State the blood parasite species.
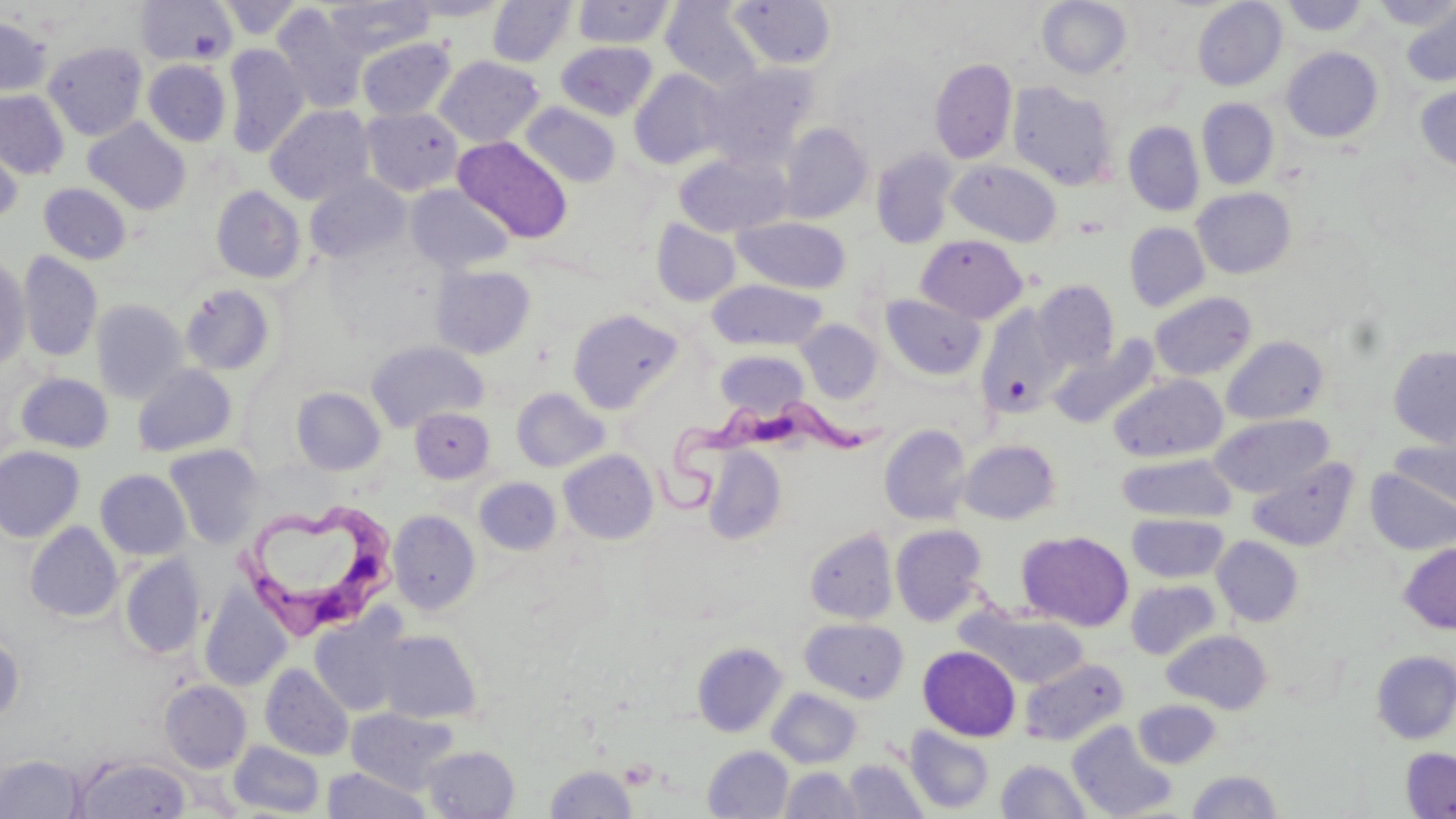
Trypanosoma brucei.

Approximate bounding boxes as (x1,y1)-(x2,y2) corner pairs in pixels. Uninfected red blood cell locations: (136,0)-(238,67), (217,0)-(305,40), (324,0)-(435,58), (401,0)-(511,22), (487,0)-(576,67), (1037,0)-(1132,78), (573,1)-(674,48), (659,1)-(765,91), (728,1)-(837,70), (1192,1)-(1287,91), (1282,1)-(1370,37), (1373,1)-(1456,30), (272,3)-(368,114), (1400,4)-(1456,88), (0,16)-(51,97), (357,37)-(456,121), (556,41)-(657,120), (44,42)-(147,140), (223,44)-(309,158), (1282,47)-(1383,142), (434,55)-(544,147), (930,58)-(1017,164), (143,59)-(231,147), (701,64)-(818,166), (629,69)-(730,170), (1008,82)-(1119,191), (1414,83)-(1456,173), (0,90)-(70,179), (1196,98)-(1279,189), (520,103)-(621,187), (265,105)-(375,205), (361,107)-(463,195), (83,118)-(191,214), (1123,121)-(1204,216), (779,123)-(872,223), (0,128)-(24,229), (453,137)-(573,243), (871,149)-(957,249), (674,152)-(791,237), (948,160)-(1062,247), (307,175)-(410,264), (39,183)-(131,264), (406,184)-(515,274), (211,187)-(305,283), (1192,187)-(1296,278), (732,216)-(851,293), (651,218)-(741,306), (1124,223)-(1210,312), (917,234)-(1028,323), (18,251)-(102,362), (0,256)-(31,370), (431,265)-(535,358), (707,280)-(828,350), (1032,280)-(1119,371), (180,283)-(276,376), (1149,291)-(1257,381), (881,294)-(986,380), (91,299)-(188,404), (977,305)-(1067,419), (567,307)-(684,413), (796,319)-(883,402), (1049,335)-(1160,428), (1221,336)-(1329,424), (366,340)-(487,431), (1388,345)-(1456,447), (715,350)-(810,418), (132,363)-(237,457), (15,373)-(114,454), (1109,373)-(1228,462), (291,387)-(386,476), (511,387)-(609,472), (409,407)-(494,484), (1210,414)-(1333,498), (879,424)-(973,525), (1388,438)-(1456,517), (958,439)-(1061,524), (164,444)-(265,549), (702,445)-(787,544), (0,446)-(84,543), (559,449)-(658,544), (1117,453)-(1236,523), (1247,457)-(1358,551), (1366,467)-(1456,555), (95,469)-(191,560), (475,477)-(561,554), (388,510)-(481,615), (1127,513)-(1228,583), (25,522)-(122,622), (890,524)-(988,625), (804,528)-(897,624), (1018,530)-(1133,631), (1212,535)-(1304,626), (1399,541)-(1456,633), (119,555)-(206,659), (1126,580)-(1220,659), (199,586)-(292,692), (961,607)-(1090,689), (311,612)-(409,717), (800,618)-(909,703), (374,630)-(482,724), (1162,630)-(1272,713), (0,632)-(25,725), (692,642)-(788,737), (918,645)-(1021,741), (1371,650)-(1456,744), (1021,658)-(1129,746), (261,664)-(353,760), (160,680)-(252,772), (767,687)-(862,768), (1133,699)-(1221,768), (347,708)-(459,792), (1066,719)-(1177,818), (903,725)-(995,814), (228,740)-(325,817), (421,745)-(520,818), (702,745)-(793,819), (1400,747)-(1456,818), (75,754)-(191,817), (0,755)-(84,817), (842,759)-(928,818), (996,759)-(1091,818), (545,764)-(637,819), (780,766)-(863,817), (322,767)-(431,818), (1186,770)-(1284,818). Trypanosoma brucei locations: (646,384)-(909,514), (240,497)-(399,638). May-Grünwald-Giemsa-stained preparation. Optical microscopy. Single field of view. Thin blood smear. Captured at 1000x magnification. Image is 1456×819 pixels.